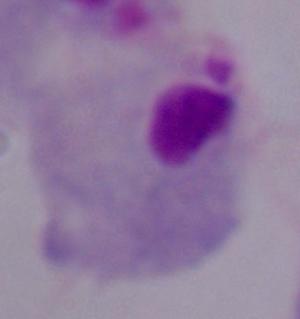
A trichomonad is shown. 1000x magnification. Photomicrograph.